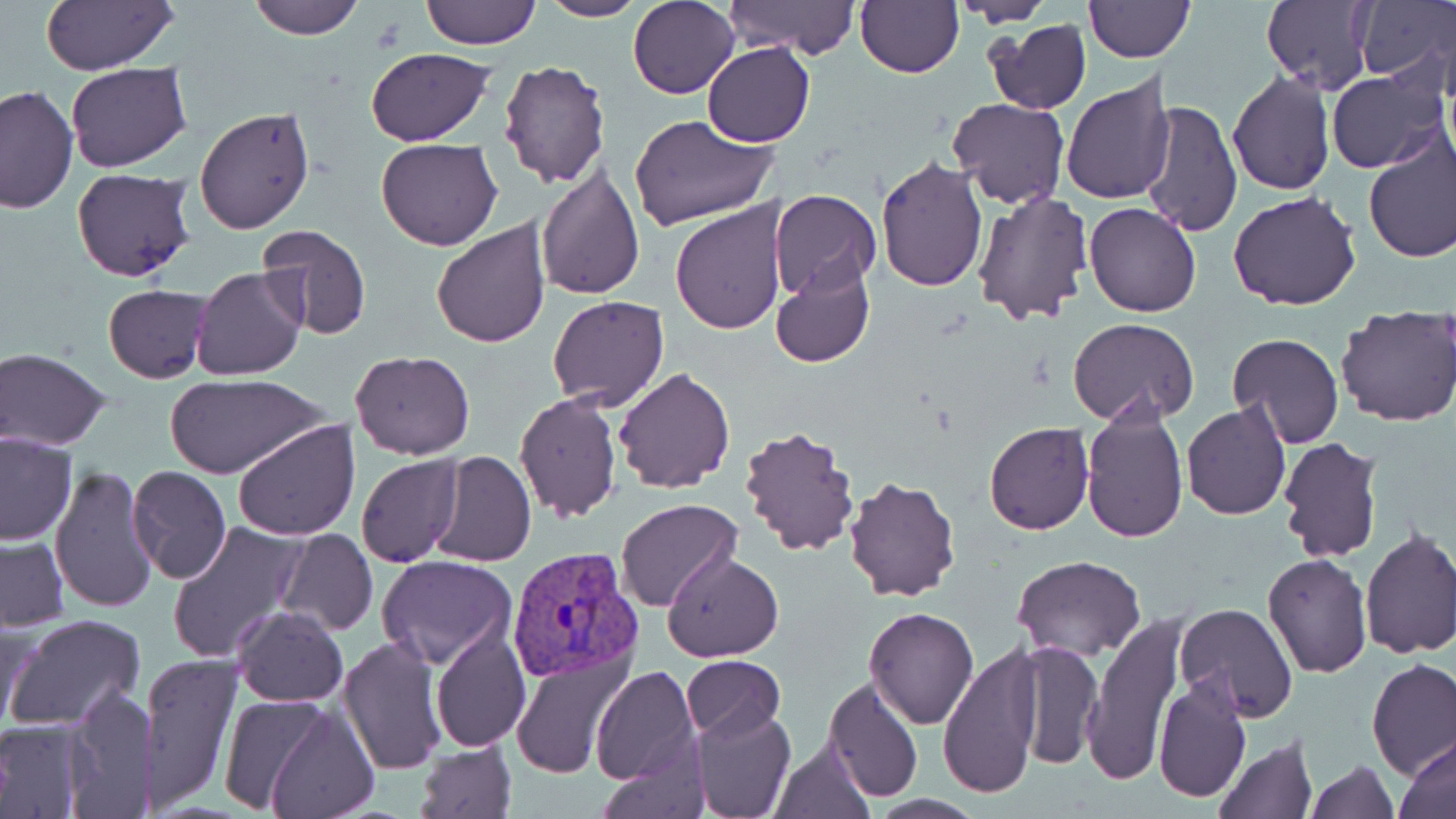 Approximate bounding boxes as [x1, y1, x2, y2] in pixels. Uninfected red blood cell locations: [246, 0, 362, 39], [419, 0, 540, 50], [538, 0, 648, 22], [630, 0, 740, 100], [855, 0, 964, 79], [1260, 0, 1375, 94], [1352, 0, 1455, 91], [40, 1, 179, 75], [722, 1, 862, 63], [1083, 1, 1193, 64], [954, 2, 1055, 25], [984, 19, 1091, 115], [702, 41, 816, 147], [364, 47, 497, 144], [499, 61, 609, 188], [65, 64, 192, 172], [1227, 70, 1335, 194], [1328, 70, 1449, 173], [1061, 75, 1178, 207], [0, 85, 76, 214], [949, 98, 1068, 208], [1139, 98, 1243, 238], [194, 106, 314, 233], [629, 114, 775, 232], [1362, 133, 1456, 265], [375, 136, 503, 251], [876, 156, 988, 292], [535, 164, 645, 300], [72, 168, 195, 282], [769, 189, 882, 304], [970, 189, 1092, 325], [1229, 191, 1362, 312], [669, 201, 785, 335], [1084, 202, 1200, 317], [431, 220, 552, 349], [253, 226, 372, 341], [769, 259, 876, 368], [191, 266, 308, 382], [103, 286, 209, 382], [548, 295, 670, 411], [1335, 306, 1456, 428], [1068, 318, 1199, 426], [1225, 333, 1344, 448], [1, 348, 113, 451], [348, 350, 474, 458], [613, 366, 735, 495], [165, 371, 326, 479], [514, 392, 623, 522], [1182, 403, 1291, 521], [1080, 405, 1189, 542], [233, 420, 361, 539], [984, 422, 1094, 535], [737, 423, 860, 558], [1, 432, 76, 544], [1276, 437, 1384, 564], [430, 451, 536, 567], [356, 455, 462, 567], [50, 467, 158, 613], [126, 467, 231, 583], [844, 475, 961, 604], [616, 498, 742, 613], [166, 519, 308, 664], [274, 528, 377, 637], [1358, 529, 1456, 660], [1, 536, 70, 630], [663, 551, 784, 661], [1012, 554, 1146, 660], [1262, 554, 1372, 677], [376, 555, 517, 670], [1175, 601, 1299, 721], [232, 606, 348, 707], [863, 607, 980, 730], [1083, 612, 1185, 787], [5, 613, 147, 733], [0, 616, 36, 737], [430, 626, 530, 752], [336, 635, 449, 776], [1012, 639, 1101, 769], [936, 643, 1045, 799], [511, 651, 633, 780], [142, 653, 242, 809], [681, 656, 784, 744], [1367, 660, 1456, 781], [591, 665, 701, 787], [1153, 675, 1252, 804], [822, 677, 924, 802], [65, 683, 159, 814], [260, 700, 380, 819], [689, 706, 797, 819], [0, 718, 89, 818], [1399, 734, 1456, 816], [769, 737, 875, 819], [1213, 737, 1317, 818], [415, 741, 517, 818], [1303, 760, 1399, 818]. Plasmodium vivax-infected red blood cell locations: [503, 546, 644, 684]. Slide-level diagnosis: Plasmodium vivax. May-Grünwald-Giemsa-stained preparation. Captured at 1000x magnification. Thin blood film. Optical microscopy. Image is 1456×819 pixels. Single field of view.